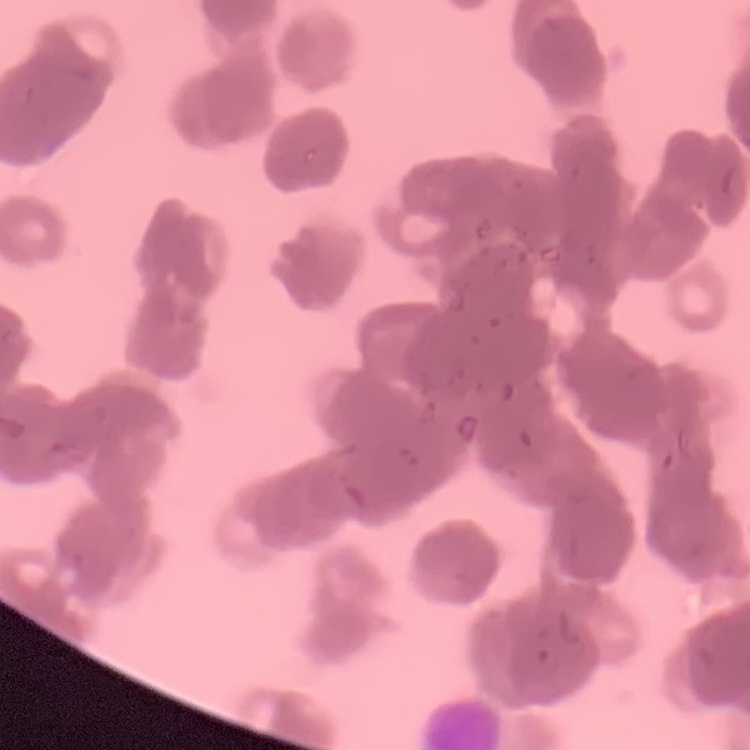

Summary:
  - Red blood cell morphology: rouleaux formation
  - Image type: one tile cut from a larger photomicrograph
  - Stain: Field's or Giemsa
  - Preparation: thin blood smear